Assess the morphology of the red blood cells.
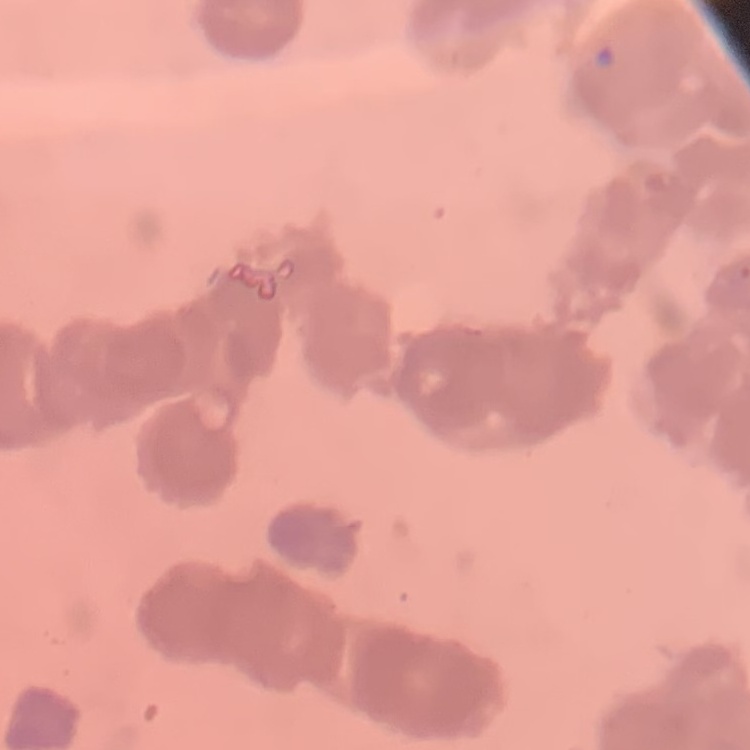
They show rouleaux formation.

Stained with either Field's or Giemsa. Thin peripheral smear. Square crop of a larger photomicrograph.